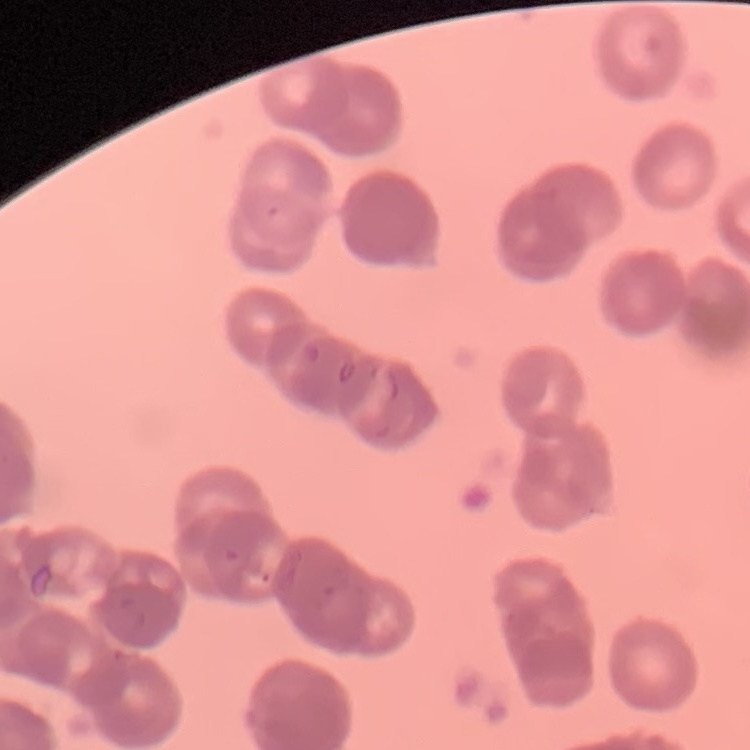

The red blood cells show rouleaux formation. Thin peripheral smear. Field's or Giemsa stain. One tile cut from a larger photomicrograph.